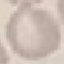
result = no malaria parasites detected
capture = smartphone through the microscope eyepiece
image type = cell patch, automatically extracted from a larger field of view and resized to 64 × 64 pixels
preparation = thin blood film
stain = Giemsa